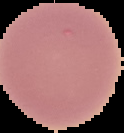

Cell region segmented out of the field of view; the surrounding area is masked to black. From a thin blood smear. Malaria status: uninfected. Image is 124×133 pixels.